Classify this cell by malaria status.
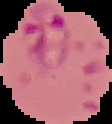
Parasitized.

preparation = thin blood film
image size = 112×124 pixels
image type = cell region segmented out of the field of view; surrounding area masked to black